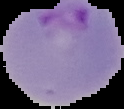

{
  "image_type": "segmented cell region with the area outside set to black",
  "preparation": "thin blood smear",
  "image_size": "124×109 pixels",
  "malaria_status": "parasitized"
}